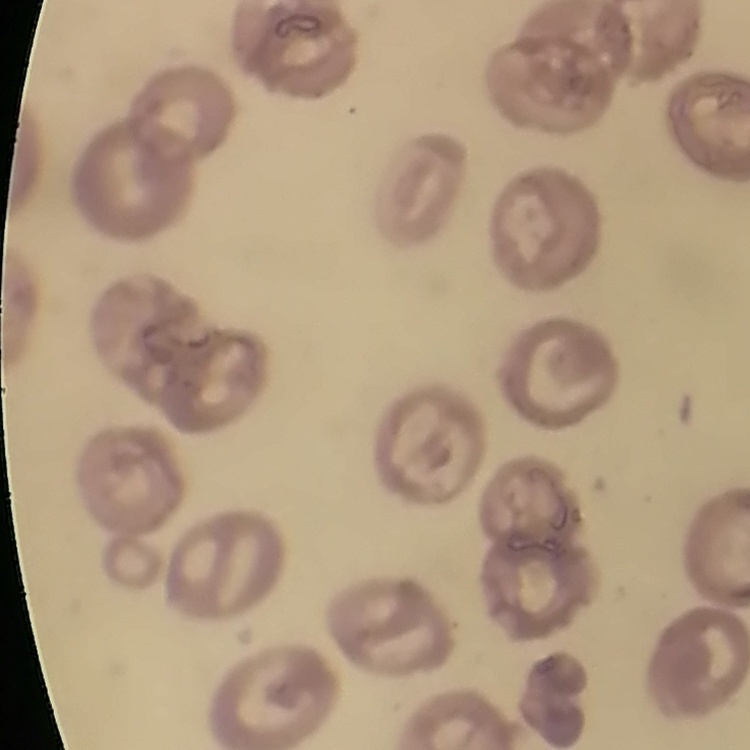
Summary:
  - Erythrocyte morphology: no rouleaux formation
  - Image type: one tile cut from a larger photomicrograph
  - Preparation: thin blood smear
  - Stain: Field's or Giemsa